Outline each uninfected red blood cell.
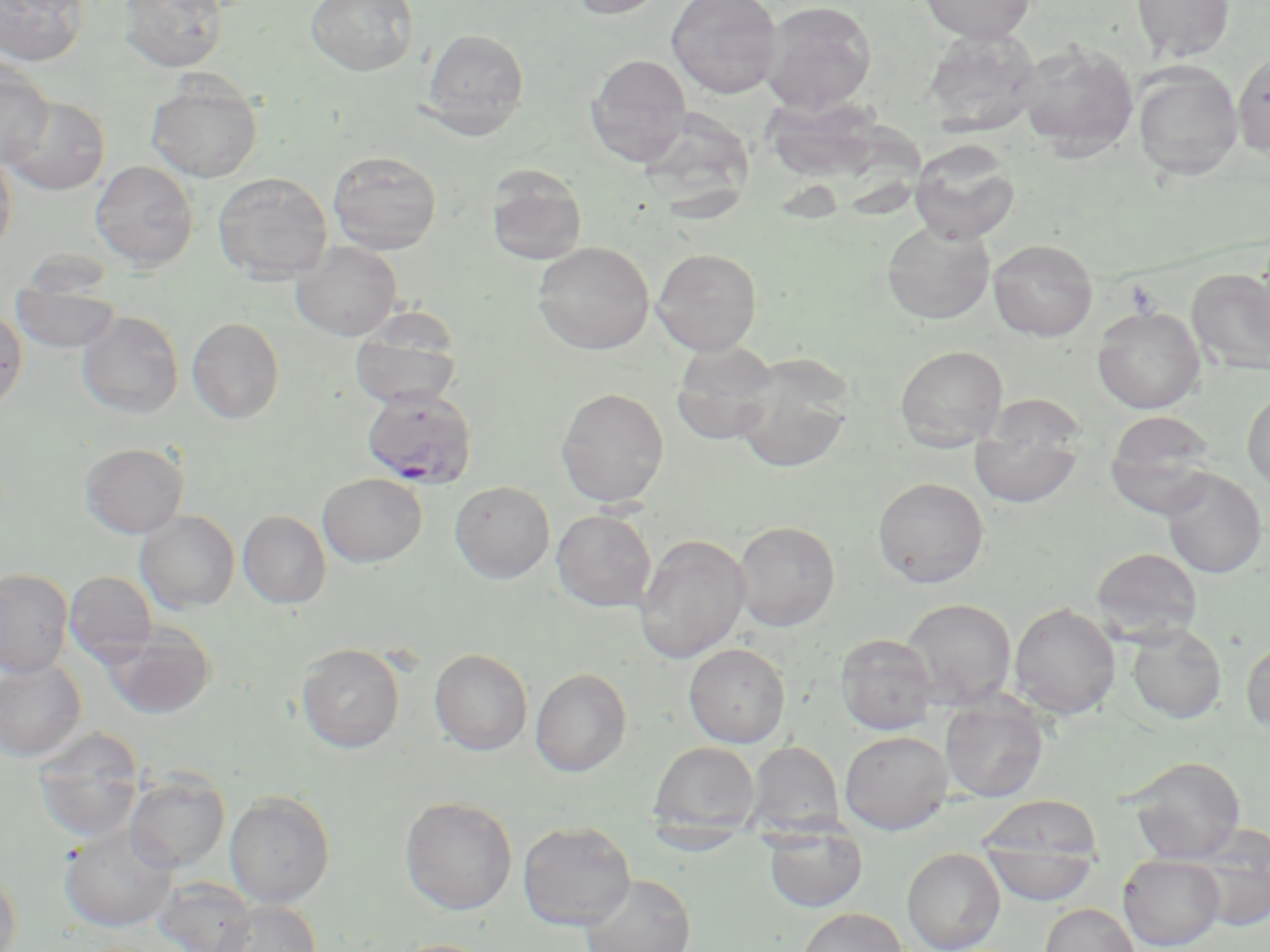
Approximate bounding boxes as (x1, y1, x2, y2) in pixels.
Uninfected red blood cells: (1, 0, 89, 66), (119, 0, 228, 73), (305, 0, 419, 76), (568, 0, 670, 20), (666, 0, 782, 99), (759, 0, 878, 114), (918, 0, 1038, 44), (1130, 0, 1235, 63), (422, 28, 530, 139), (922, 28, 1042, 136), (1017, 39, 1140, 158), (1232, 51, 1270, 157), (585, 54, 692, 166), (0, 58, 54, 166), (1132, 64, 1243, 181), (147, 77, 263, 182), (762, 92, 884, 197), (3, 95, 110, 195), (644, 107, 761, 224), (839, 127, 938, 235), (909, 139, 1020, 245), (0, 148, 17, 258), (327, 150, 442, 254), (90, 160, 198, 270), (486, 164, 588, 266), (212, 171, 332, 283), (881, 221, 995, 324), (988, 238, 1098, 342), (533, 241, 654, 355), (291, 242, 402, 341), (651, 248, 762, 355), (1187, 268, 1270, 375), (12, 279, 122, 353), (1093, 306, 1205, 414), (0, 308, 27, 414), (77, 311, 184, 418), (187, 317, 284, 424), (349, 321, 462, 411), (670, 341, 781, 446), (894, 346, 1008, 452), (731, 355, 853, 474), (556, 388, 669, 507), (1242, 388, 1270, 493), (1104, 411, 1218, 515), (970, 420, 1083, 509), (80, 442, 189, 538), (1161, 469, 1268, 578), (318, 473, 427, 566), (873, 476, 989, 588), (449, 480, 555, 583), (551, 509, 657, 612), (136, 511, 239, 612), (238, 511, 331, 608), (733, 521, 840, 631), (634, 533, 750, 664), (1091, 547, 1203, 641), (0, 569, 73, 678), (64, 571, 157, 665), (902, 598, 1018, 709), (1009, 602, 1120, 719), (103, 623, 216, 719), (1126, 624, 1227, 724), (835, 633, 938, 735), (1241, 638, 1270, 734), (297, 643, 405, 754), (684, 643, 790, 747), (429, 648, 533, 756), (0, 660, 86, 762), (531, 668, 631, 776), (940, 696, 1049, 802), (33, 729, 144, 843), (840, 730, 953, 834), (746, 740, 844, 836), (649, 741, 759, 835), (1125, 756, 1246, 862), (125, 771, 230, 873), (225, 791, 335, 907), (977, 795, 1105, 892), (400, 796, 517, 915), (517, 820, 636, 930), (761, 822, 869, 913), (60, 824, 178, 932), (1187, 828, 1270, 933), (980, 839, 1100, 908), (902, 847, 1006, 952), (1118, 854, 1226, 950), (0, 867, 22, 952), (580, 873, 696, 952), (153, 876, 257, 952), (212, 900, 322, 952), (1039, 903, 1139, 952), (796, 907, 908, 952), (388, 938, 504, 952).

Platelet locations: (1124, 279, 1163, 318). Plasmodium falciparum-infected red blood cell locations: (360, 385, 479, 490). Slide-level diagnosis: Plasmodium falciparum. One field of a larger specimen. Light microscopy. Captured at 1000x magnification. Thin blood film. Image is 1270×952 pixels. May-Grünwald-Giemsa stain.